Give the extent of all Plasmodium malariae-infected red blood cells.
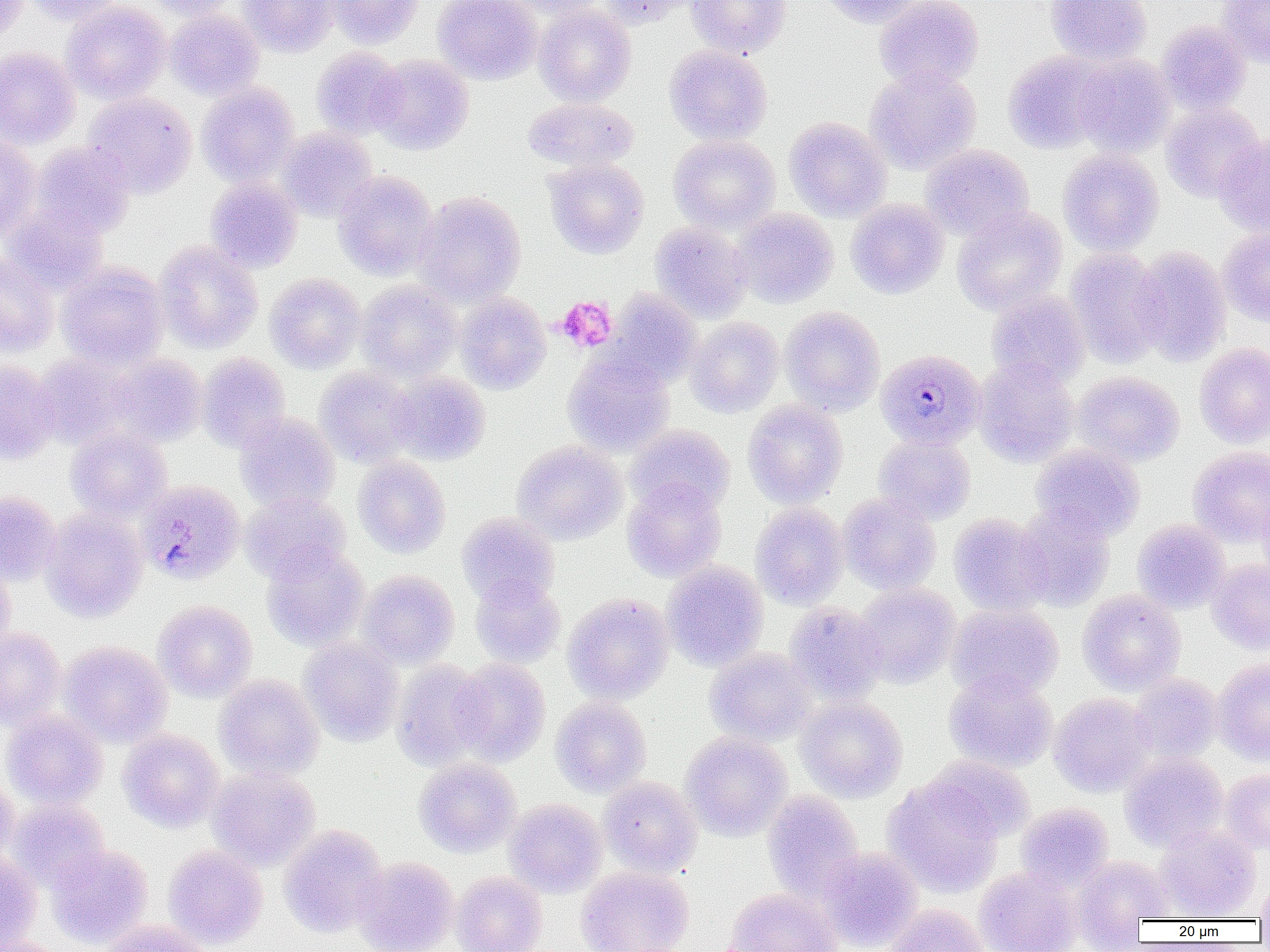
Approximate bounding boxes as [x1, y1, x2, y2] in pixels.
Plasmodium malariae-infected red blood cells: [876, 348, 986, 450], [137, 479, 245, 586].

slide-level diagnosis = Plasmodium malariae
magnification = 1000x
uninfected red blood cell locations = approximate bounding boxes as [x1, y1, x2, y2] in pixels: [0, 0, 29, 43], [23, 0, 124, 25], [145, 0, 241, 20], [238, 0, 337, 57], [327, 0, 424, 49], [433, 0, 543, 84], [508, 0, 609, 19], [600, 0, 694, 28], [687, 0, 792, 58], [820, 0, 926, 28], [874, 0, 984, 90], [1044, 0, 1152, 66], [1216, 0, 1270, 66], [61, 1, 170, 104], [533, 5, 636, 106], [165, 9, 264, 101], [1157, 21, 1251, 114], [664, 45, 772, 145], [0, 46, 81, 149], [311, 47, 406, 139], [1003, 50, 1111, 154], [370, 54, 474, 155], [1072, 55, 1176, 157], [865, 66, 982, 174], [197, 82, 299, 186], [83, 92, 197, 198], [522, 97, 639, 173], [1161, 102, 1265, 202], [784, 117, 892, 222], [276, 127, 377, 222], [1213, 132, 1270, 236], [0, 134, 41, 238], [668, 134, 781, 234], [31, 142, 135, 239], [920, 144, 1034, 240], [1058, 148, 1164, 256], [544, 158, 649, 259], [347, 170, 447, 379], [333, 171, 438, 281], [205, 178, 302, 272], [413, 191, 526, 306], [846, 199, 949, 299], [2, 203, 108, 295], [952, 206, 1067, 314], [731, 207, 839, 308], [650, 222, 752, 322], [1218, 228, 1270, 327], [154, 241, 263, 353], [1065, 247, 1168, 368], [1132, 247, 1232, 366], [0, 254, 59, 357], [56, 262, 168, 371], [265, 273, 366, 373], [356, 280, 462, 382], [604, 290, 702, 389], [986, 290, 1090, 389], [455, 291, 551, 393], [780, 306, 885, 416], [686, 317, 784, 417], [1194, 343, 1270, 448], [562, 352, 675, 457], [33, 353, 137, 448], [197, 353, 290, 452], [111, 354, 207, 447], [974, 357, 1080, 467], [0, 360, 60, 464], [315, 367, 417, 466], [1072, 371, 1184, 466], [387, 372, 490, 465], [742, 400, 848, 508], [235, 413, 340, 513], [626, 424, 735, 516], [66, 425, 171, 521], [873, 433, 976, 525], [512, 440, 627, 544], [1031, 443, 1145, 541], [1188, 446, 1270, 546], [353, 455, 451, 558], [622, 479, 726, 582], [1257, 487, 1270, 581], [0, 491, 61, 585], [241, 491, 350, 582], [838, 494, 941, 594], [750, 502, 849, 609], [1014, 502, 1115, 611], [41, 508, 148, 623], [457, 513, 560, 608], [948, 513, 1051, 616], [1132, 519, 1231, 614], [261, 543, 368, 650], [1206, 559, 1270, 655], [662, 560, 769, 671], [0, 561, 15, 655], [357, 570, 459, 668], [471, 576, 565, 667], [854, 582, 961, 688], [1077, 590, 1186, 695], [563, 593, 674, 703], [153, 600, 257, 702], [785, 602, 887, 705], [946, 603, 1063, 700], [0, 627, 66, 730], [299, 637, 404, 746], [59, 641, 171, 746], [705, 647, 816, 747], [449, 658, 551, 766], [1213, 658, 1270, 765], [390, 659, 491, 770], [944, 669, 1057, 772], [1129, 673, 1223, 764], [214, 674, 324, 781], [1049, 693, 1155, 797], [550, 696, 651, 797], [796, 696, 907, 802], [1, 709, 108, 809], [118, 728, 225, 832], [680, 732, 792, 841], [1120, 752, 1228, 852], [926, 755, 1035, 843], [413, 758, 521, 857], [207, 767, 321, 871], [1221, 767, 1270, 854], [0, 776, 19, 868], [598, 776, 702, 877], [883, 777, 1004, 897], [763, 791, 864, 902], [8, 798, 110, 891], [503, 799, 607, 897], [1015, 803, 1114, 894], [279, 824, 387, 937], [1155, 826, 1261, 920], [47, 844, 154, 949], [163, 845, 268, 949], [817, 848, 923, 950], [0, 851, 43, 951], [1071, 855, 1174, 941], [353, 856, 458, 952], [576, 865, 693, 952], [974, 868, 1080, 952], [451, 871, 547, 952], [1255, 875, 1270, 922], [725, 888, 842, 952], [884, 904, 990, 952], [97, 919, 212, 952], [1, 936, 71, 952]
field of view = single
modality = optical microscopy
preparation = thin blood smear
platelet locations = approximate bounding boxes as [x1, y1, x2, y2] in pixels: [557, 296, 617, 353]
image size = 1270×952 pixels